Comment on the morphology of the erythrocytes.
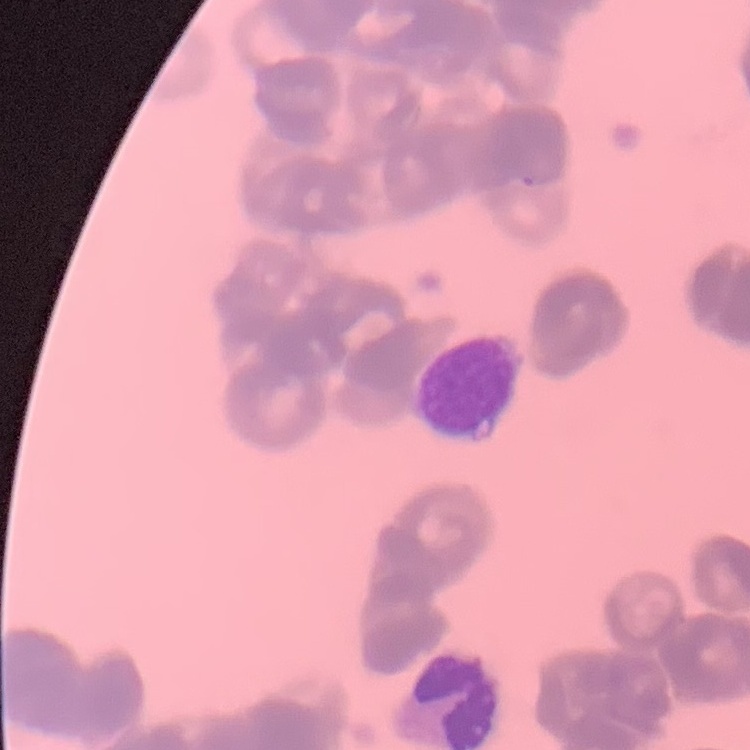

They show rouleaux formation.

Thin blood smear. Field's or Giemsa stain. One tile cut from a larger photomicrograph.